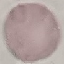 Result: negative for malaria parasites. Thin blood smear. Acquired by smartphone through the microscope eyepiece. Cell patch, automatically extracted from a larger field of view and resized to 64 × 64 pixels. Giemsa-stained preparation.